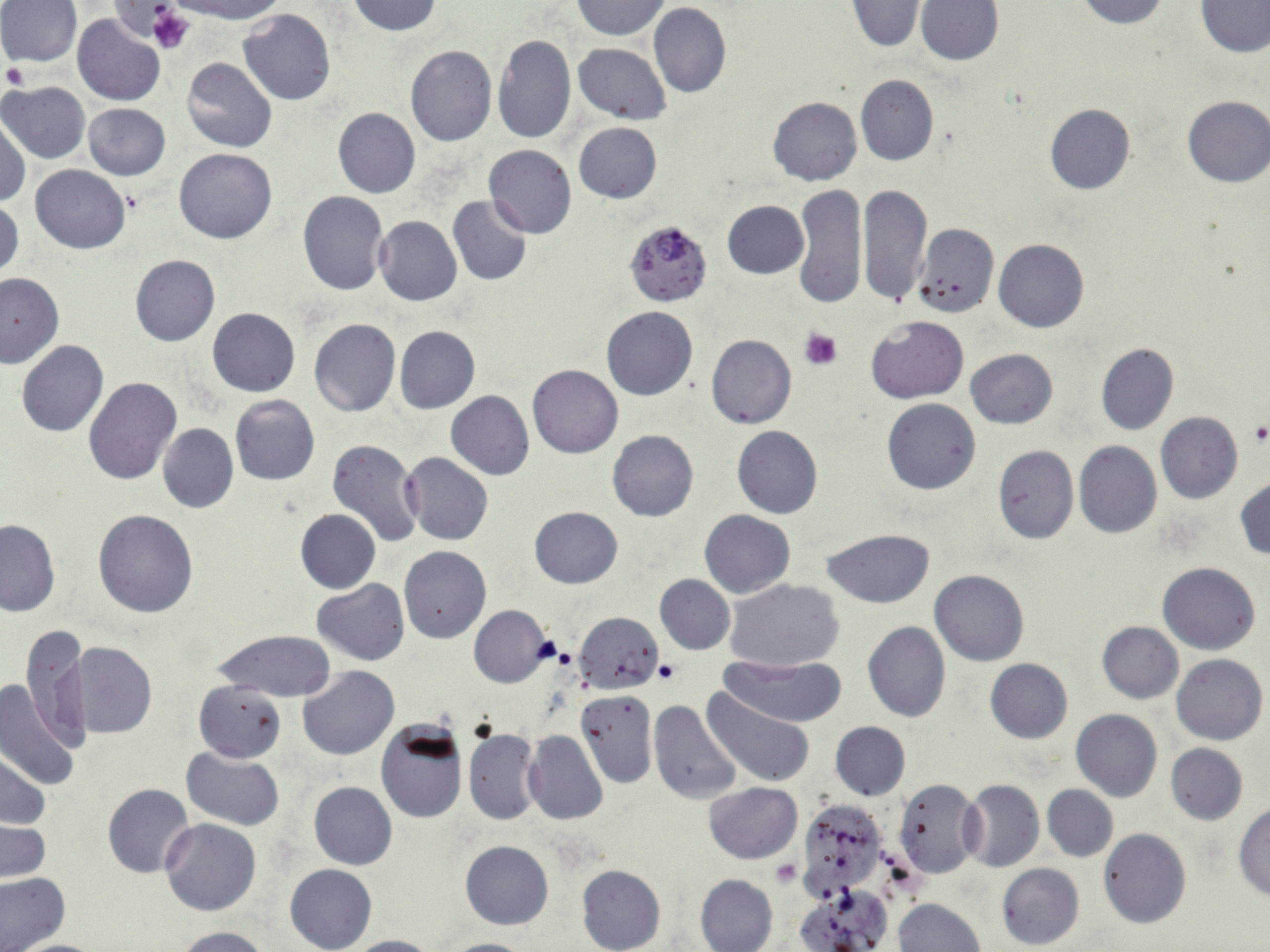
{
  "slide_level_diagnosis": "Plasmodium falciparum",
  "modality": "light microscopy",
  "image_size": "1270×952 pixels",
  "plasmodium_falciparum_infected_red_blood_cell_locations": "approximate bounding boxes as (x1, y1, x2, y2) in pixels: (625, 220, 714, 307)",
  "field_of_view": "one of a larger specimen",
  "platelet_locations": "approximate bounding boxes as (x1, y1, x2, y2) in pixels: (147, 5, 196, 55), (2, 62, 29, 90), (800, 326, 843, 371), (1247, 421, 1270, 444), (654, 659, 681, 684), (773, 860, 800, 886)",
  "magnification": "1000x",
  "stain": "May-Grünwald-Giemsa",
  "preparation": "thin blood film",
  "uninfected_red_blood_cell_locations": "approximate bounding boxes as (x1, y1, x2, y2) in pixels: (167, 0, 288, 23), (348, 0, 442, 36), (571, 0, 670, 38), (1077, 0, 1167, 27), (0, 1, 81, 68), (916, 1, 1002, 66), (1198, 1, 1270, 57), (848, 2, 923, 50), (648, 4, 731, 99), (239, 10, 336, 105), (73, 14, 164, 106), (492, 33, 576, 145), (573, 43, 671, 124), (405, 46, 496, 147), (182, 57, 277, 153), (856, 74, 939, 165), (0, 82, 90, 164), (1181, 95, 1269, 187), (767, 96, 861, 186), (83, 103, 170, 180), (1045, 103, 1136, 194), (333, 108, 420, 198), (0, 117, 30, 208), (574, 122, 662, 203), (483, 145, 576, 238), (175, 148, 276, 243), (30, 165, 131, 253), (793, 183, 867, 309), (859, 183, 932, 307), (298, 191, 389, 295), (448, 195, 531, 286), (1, 196, 23, 283), (723, 200, 808, 278), (373, 215, 461, 305), (914, 224, 999, 317), (994, 239, 1089, 332), (130, 254, 220, 346), (0, 272, 67, 367), (602, 306, 697, 400), (208, 308, 300, 396), (865, 315, 968, 404), (309, 319, 400, 416), (394, 325, 480, 414), (706, 334, 796, 429), (17, 341, 107, 436), (1095, 343, 1178, 434), (966, 348, 1058, 429), (527, 364, 622, 457), (84, 377, 182, 486), (445, 390, 534, 480), (230, 395, 320, 486), (882, 399, 981, 495), (1155, 411, 1242, 504), (158, 423, 238, 512), (731, 426, 823, 518), (607, 430, 699, 521), (326, 439, 424, 549), (1074, 441, 1161, 538), (991, 445, 1077, 544), (402, 451, 493, 545), (1235, 476, 1270, 560), (529, 506, 622, 588), (94, 508, 199, 617), (295, 509, 380, 593), (700, 510, 795, 598), (0, 518, 60, 615), (822, 529, 933, 607), (399, 547, 491, 644), (1158, 562, 1260, 654), (930, 569, 1029, 666), (655, 575, 735, 654), (725, 578, 843, 670), (311, 580, 410, 665), (469, 606, 552, 687), (573, 611, 664, 693), (863, 621, 951, 721), (20, 622, 92, 754), (1096, 622, 1183, 703), (211, 629, 336, 702), (64, 642, 158, 739), (1172, 654, 1267, 745), (725, 655, 845, 726), (985, 659, 1072, 743), (298, 665, 399, 760), (0, 679, 82, 792), (193, 680, 286, 763), (701, 687, 814, 788), (575, 689, 657, 788), (649, 700, 742, 805), (1071, 709, 1163, 802), (376, 720, 467, 823), (830, 722, 910, 800), (463, 727, 542, 825), (523, 730, 608, 825), (1165, 743, 1247, 825), (181, 747, 286, 830), (1, 750, 50, 831), (894, 779, 984, 878), (960, 779, 1044, 871), (309, 782, 396, 870), (704, 782, 801, 862), (102, 783, 195, 878), (1043, 785, 1118, 861), (799, 800, 889, 898), (1232, 804, 1270, 901), (160, 819, 261, 916), (1, 821, 49, 883), (1099, 829, 1191, 928), (461, 841, 553, 929), (997, 863, 1084, 950), (285, 864, 377, 952), (577, 865, 665, 952), (695, 873, 778, 952), (0, 874, 72, 952), (797, 888, 891, 952), (893, 898, 985, 952), (175, 927, 271, 952), (340, 934, 439, 952), (14, 938, 104, 951), (434, 938, 536, 952)"
}